Assess this cell for malaria.
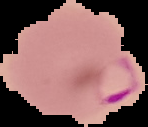
Parasitized.

{
  "preparation": "thin blood smear",
  "image_type": "cell region segmented out of the field of view; surrounding area masked to black",
  "image_size": "148×127 pixels"
}